Name the parasite shown.
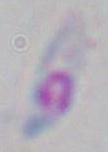

Toxoplasma gondii.

magnification = 1000x
modality = photomicrograph